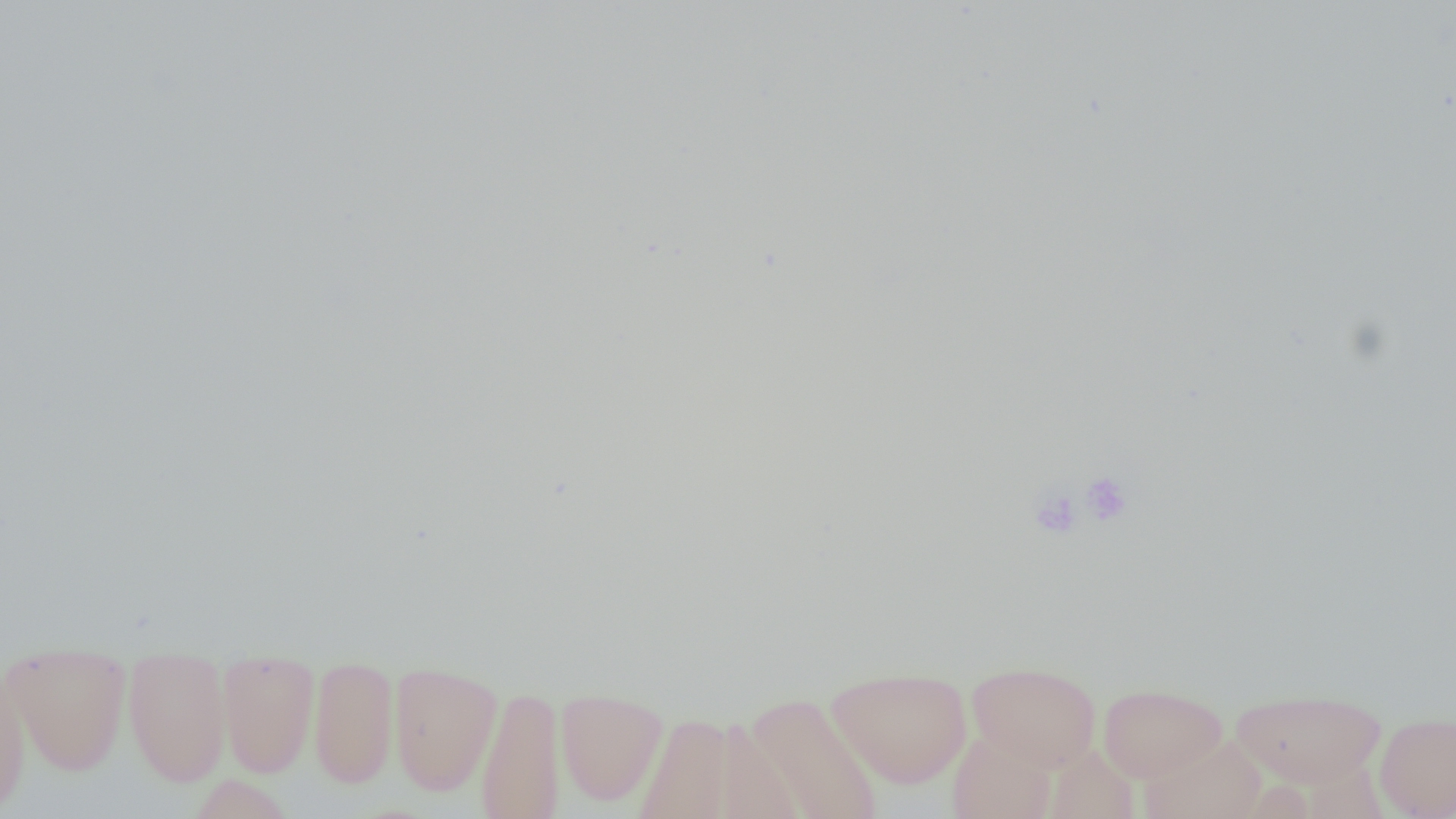

slide_level_diagnosis: negative for blood parasites
magnification: 1000x
image_size: 1456×819 pixels
preparation: thin blood film
field_of_view: single
platelet_locations: 'approximate bounding boxes as [x1, y1, x2, y2] in pixels: [1080, 470, 1134, 527], [1028, 487, 1083, 540]'
modality: optical microscopy
uninfected_red_blood_cell_locations: 'approximate bounding boxes as [x1, y1, x2, y2] in pixels: [2, 643, 132, 776], [309, 654, 399, 790], [122, 655, 232, 786], [217, 655, 320, 778], [388, 661, 502, 796], [968, 661, 1101, 772], [0, 663, 31, 815], [827, 667, 971, 788], [1098, 683, 1227, 782], [475, 685, 565, 819], [1230, 687, 1386, 788], [556, 688, 668, 807], [743, 692, 883, 819], [629, 711, 757, 818], [1375, 712, 1456, 818], [947, 729, 1057, 819], [1140, 734, 1267, 819], [1044, 744, 1140, 818], [187, 773, 296, 819]'